Assess the morphology of the erythrocytes.
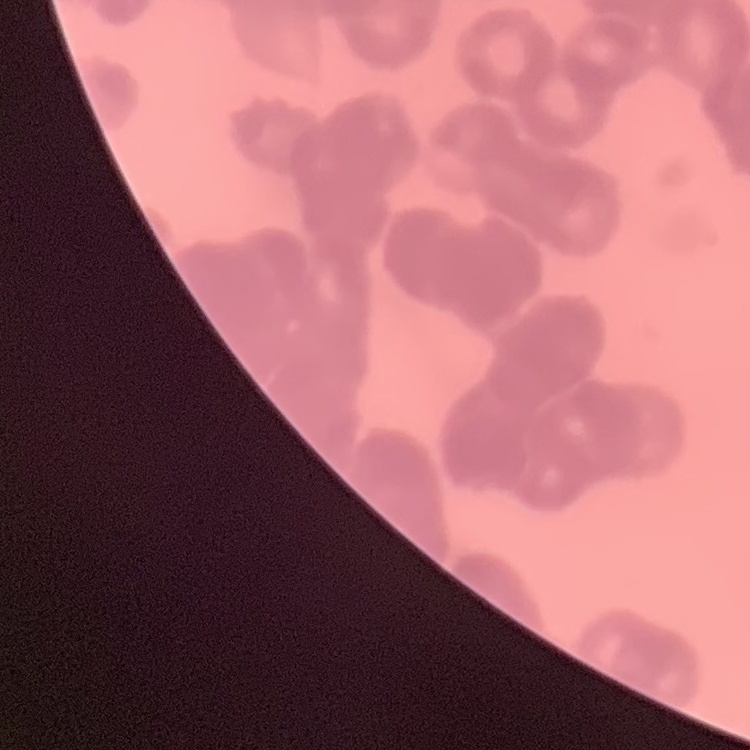

Rouleaux formation.

Thin blood film. Square crop of a larger photomicrograph. Stained with either Field's or Giemsa.